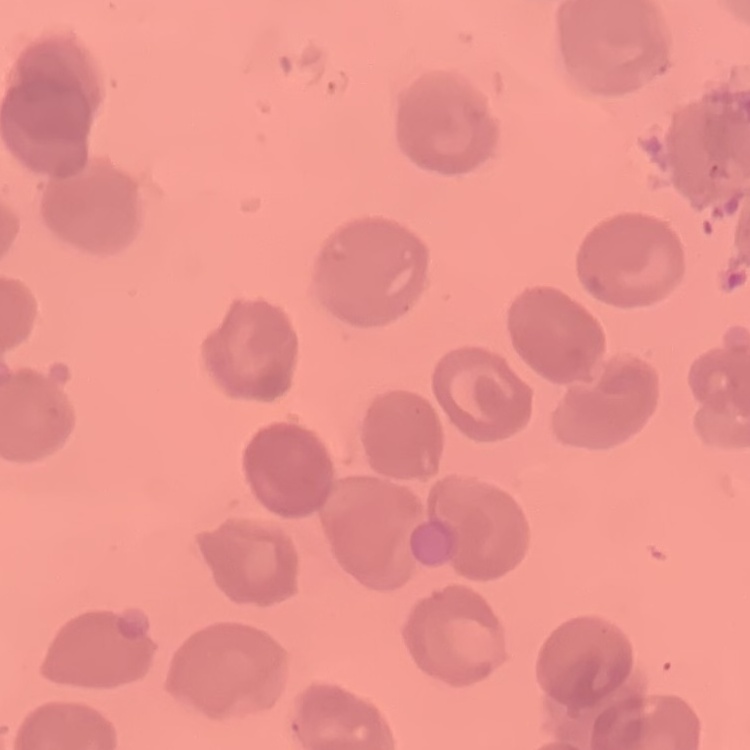
red_blood_cell_morphology: no rouleaux formation
preparation: thin blood smear
stain: Field's or Giemsa
image_type: one tile cut from a larger photomicrograph